Classify this cell by malaria status.
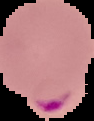

Parasitized.

{
  "image_size": "94×121 pixels",
  "image_type": "segmented cell region on a black background",
  "preparation": "thin blood smear"
}